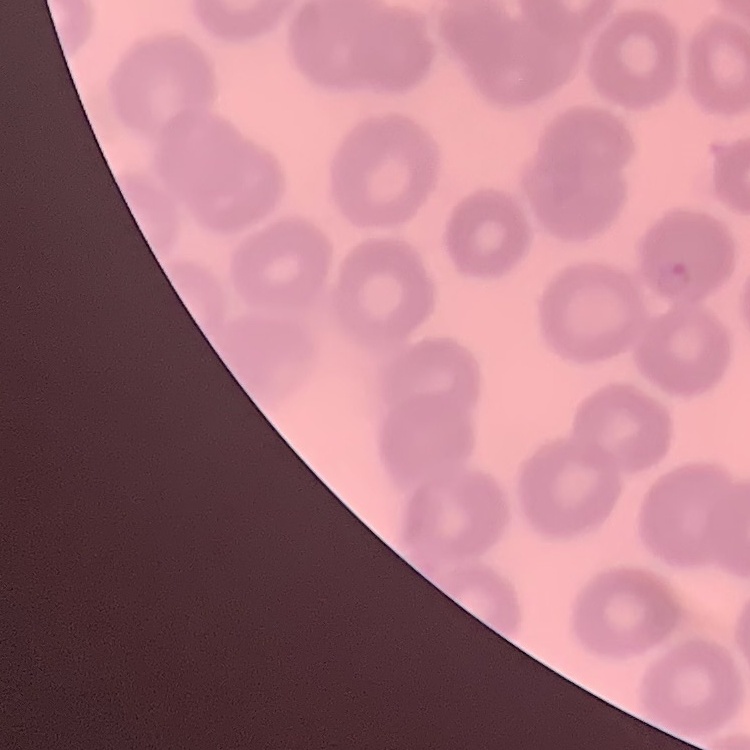

{
  "erythrocyte_morphology": "no rouleaux formation",
  "stain": "Field's or Giemsa",
  "image_type": "square crop of a larger photomicrograph",
  "preparation": "thin peripheral smear"
}